Comment on the morphology of the red blood cells.
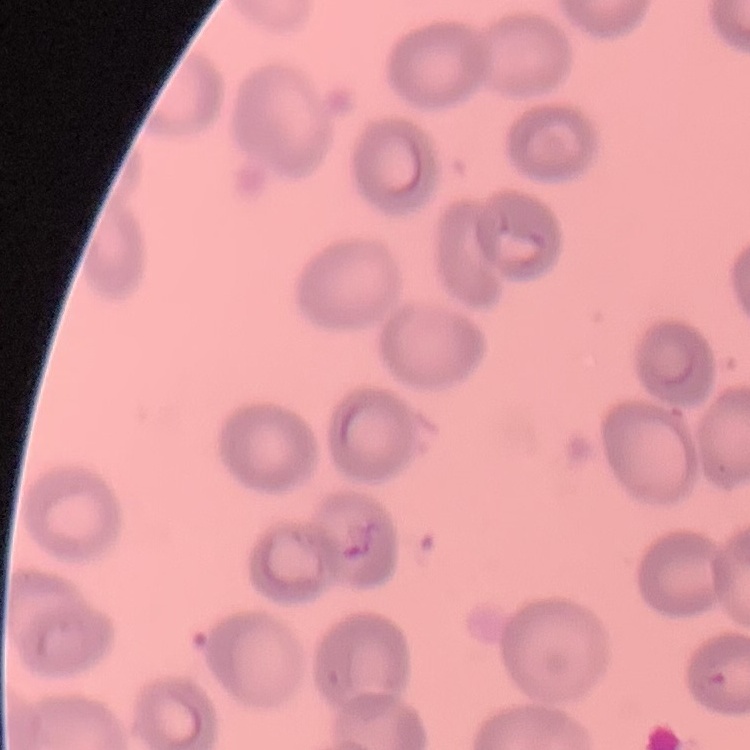

No rouleaux formation.

image type = square crop of a larger photomicrograph
preparation = thin peripheral smear
stain = Field's or Giemsa